Classify this cell by malaria status.
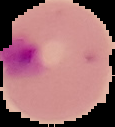
It is parasitized.

{
  "image_type": "segmented cell region with the area outside set to black",
  "preparation": "thin blood smear",
  "image_size": "115×127 pixels"
}